Classify this cell by malaria status.
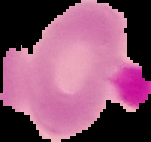
It is uninfected.

From a thin blood smear. The area outside the segmented cell region is set to black. Image is 151×142 pixels.